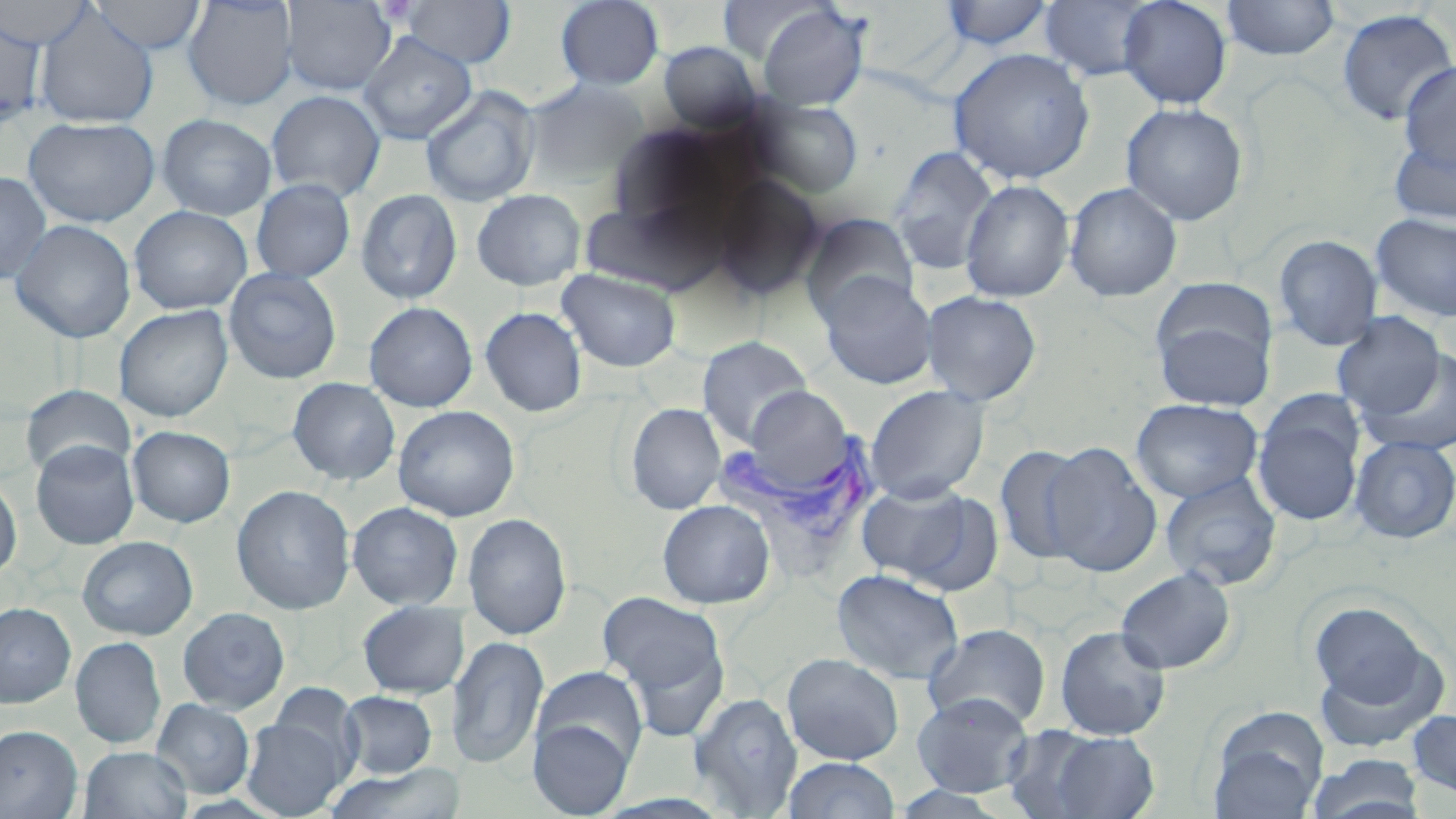 Approximate bounding boxes as named x1/y1/x2/y2 corners in pixels. Plasmodium vivax-infected red blood cell locations: (x1=709, y1=424, x2=884, y2=553). Uninfected red blood cell locations: (x1=0, y1=0, x2=97, y2=50), (x1=89, y1=0, x2=207, y2=54), (x1=182, y1=0, x2=299, y2=111), (x1=555, y1=0, x2=664, y2=90), (x1=1117, y1=0, x2=1232, y2=108), (x1=1220, y1=0, x2=1340, y2=60), (x1=281, y1=1, x2=397, y2=95), (x1=399, y1=1, x2=516, y2=69), (x1=718, y1=1, x2=826, y2=64), (x1=938, y1=1, x2=1056, y2=51), (x1=1039, y1=1, x2=1158, y2=82), (x1=756, y1=4, x2=870, y2=111), (x1=33, y1=7, x2=159, y2=128), (x1=1335, y1=8, x2=1456, y2=127), (x1=0, y1=14, x2=47, y2=130), (x1=358, y1=33, x2=477, y2=144), (x1=657, y1=41, x2=764, y2=132), (x1=948, y1=47, x2=1096, y2=184), (x1=1397, y1=62, x2=1456, y2=175), (x1=522, y1=79, x2=649, y2=188), (x1=420, y1=86, x2=540, y2=207), (x1=266, y1=90, x2=385, y2=202), (x1=749, y1=98, x2=864, y2=198), (x1=1120, y1=103, x2=1248, y2=226), (x1=156, y1=114, x2=277, y2=221), (x1=24, y1=116, x2=159, y2=227), (x1=1388, y1=132, x2=1456, y2=226), (x1=888, y1=145, x2=999, y2=276), (x1=0, y1=171, x2=52, y2=285), (x1=710, y1=175, x2=826, y2=301), (x1=251, y1=179, x2=355, y2=283), (x1=959, y1=179, x2=1075, y2=302), (x1=1064, y1=182, x2=1183, y2=302), (x1=355, y1=189, x2=462, y2=304), (x1=471, y1=189, x2=586, y2=291), (x1=579, y1=200, x2=720, y2=295), (x1=129, y1=205, x2=252, y2=314), (x1=802, y1=212, x2=919, y2=323), (x1=1370, y1=212, x2=1456, y2=322), (x1=9, y1=219, x2=135, y2=343), (x1=1273, y1=234, x2=1383, y2=351), (x1=223, y1=267, x2=342, y2=384), (x1=557, y1=269, x2=681, y2=373), (x1=818, y1=272, x2=938, y2=389), (x1=1152, y1=279, x2=1278, y2=372), (x1=921, y1=290, x2=1042, y2=406), (x1=363, y1=301, x2=478, y2=412), (x1=114, y1=305, x2=233, y2=422), (x1=479, y1=306, x2=587, y2=417), (x1=1153, y1=311, x2=1274, y2=411), (x1=1331, y1=312, x2=1446, y2=421), (x1=697, y1=336, x2=813, y2=447), (x1=1362, y1=349, x2=1455, y2=457), (x1=287, y1=377, x2=400, y2=485), (x1=21, y1=384, x2=135, y2=479), (x1=865, y1=384, x2=990, y2=503), (x1=1252, y1=396, x2=1366, y2=529), (x1=1131, y1=398, x2=1263, y2=503), (x1=625, y1=403, x2=726, y2=514), (x1=392, y1=405, x2=520, y2=521), (x1=127, y1=426, x2=236, y2=528), (x1=1349, y1=435, x2=1456, y2=544), (x1=30, y1=440, x2=140, y2=550), (x1=1040, y1=440, x2=1163, y2=578), (x1=993, y1=445, x2=1092, y2=568), (x1=1159, y1=472, x2=1283, y2=591), (x1=0, y1=473, x2=22, y2=581), (x1=854, y1=481, x2=985, y2=588), (x1=231, y1=484, x2=356, y2=615), (x1=657, y1=499, x2=775, y2=609), (x1=347, y1=501, x2=464, y2=610), (x1=462, y1=512, x2=572, y2=639), (x1=77, y1=536, x2=198, y2=640), (x1=1115, y1=566, x2=1237, y2=675), (x1=831, y1=568, x2=964, y2=685), (x1=598, y1=591, x2=728, y2=706), (x1=357, y1=601, x2=469, y2=698), (x1=1307, y1=601, x2=1438, y2=716), (x1=0, y1=602, x2=76, y2=708), (x1=177, y1=607, x2=290, y2=714), (x1=923, y1=623, x2=1051, y2=731), (x1=1054, y1=624, x2=1171, y2=740), (x1=448, y1=635, x2=549, y2=770), (x1=70, y1=636, x2=166, y2=749), (x1=1311, y1=646, x2=1446, y2=753), (x1=782, y1=652, x2=905, y2=765), (x1=532, y1=665, x2=649, y2=772), (x1=271, y1=684, x2=364, y2=777), (x1=339, y1=690, x2=438, y2=778), (x1=688, y1=692, x2=802, y2=816), (x1=910, y1=692, x2=1034, y2=797), (x1=151, y1=698, x2=255, y2=798), (x1=1207, y1=707, x2=1328, y2=818), (x1=1406, y1=709, x2=1456, y2=799), (x1=241, y1=718, x2=347, y2=818), (x1=528, y1=718, x2=634, y2=817), (x1=0, y1=725, x2=82, y2=818), (x1=1001, y1=726, x2=1115, y2=816), (x1=1045, y1=731, x2=1160, y2=818), (x1=79, y1=746, x2=192, y2=819), (x1=1308, y1=753, x2=1426, y2=819), (x1=782, y1=756, x2=901, y2=819), (x1=323, y1=762, x2=465, y2=819). Slide-level diagnosis: Plasmodium vivax. Light microscopy. Single field of view. Image is 1456×819 pixels. Thin blood film. Captured at 1000x magnification. May-Grünwald-Giemsa stain.